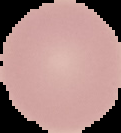
image type = segmented cell region on a black background
image size = 121×133 pixels
preparation = thin blood film
malaria status = uninfected